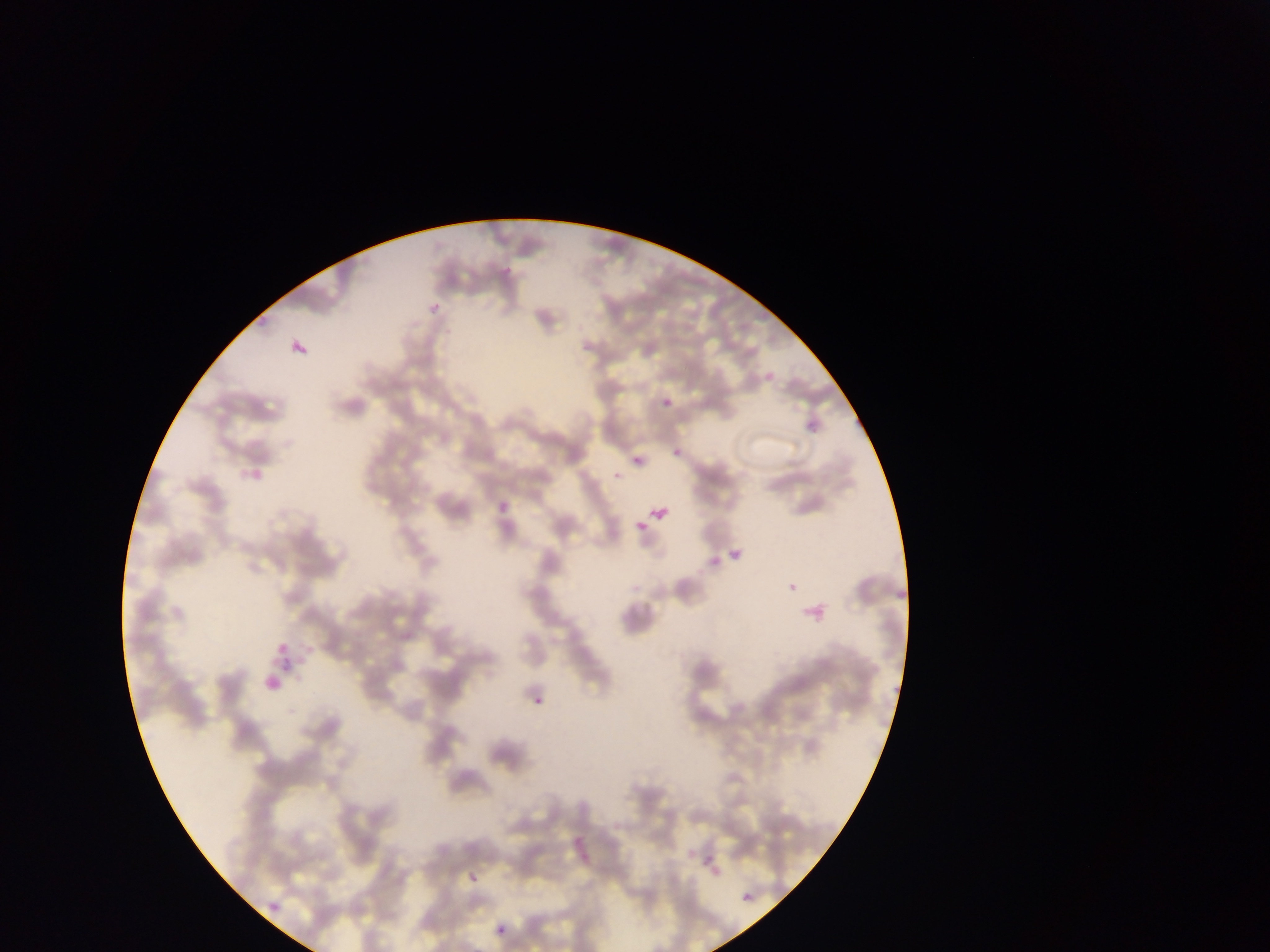 Approximate bounding boxes as {left, top, right, bottom} in pixels. Malaria parasite locations: {419, 301, 442, 318}, {289, 332, 311, 354}, {759, 367, 782, 393}, {659, 396, 671, 408}, {802, 412, 828, 432}, {620, 448, 649, 468}, {667, 448, 683, 459}, {611, 457, 630, 477}, {246, 462, 265, 490}, {493, 483, 511, 512}, {648, 499, 675, 528}, {631, 514, 646, 533}, {727, 547, 740, 565}, {781, 577, 800, 588}, {796, 599, 832, 616}, {269, 634, 294, 650}, {284, 654, 299, 671}, {261, 668, 287, 702}, {529, 689, 552, 715}, {701, 845, 729, 874}, {464, 858, 487, 882}, {740, 891, 759, 906}, {262, 892, 284, 919}, {491, 914, 514, 940}. Thin blood film. Single field of view. Mobile-phone photograph taken through the microscope. Collected in Ghana. Image is 1270×952 pixels.